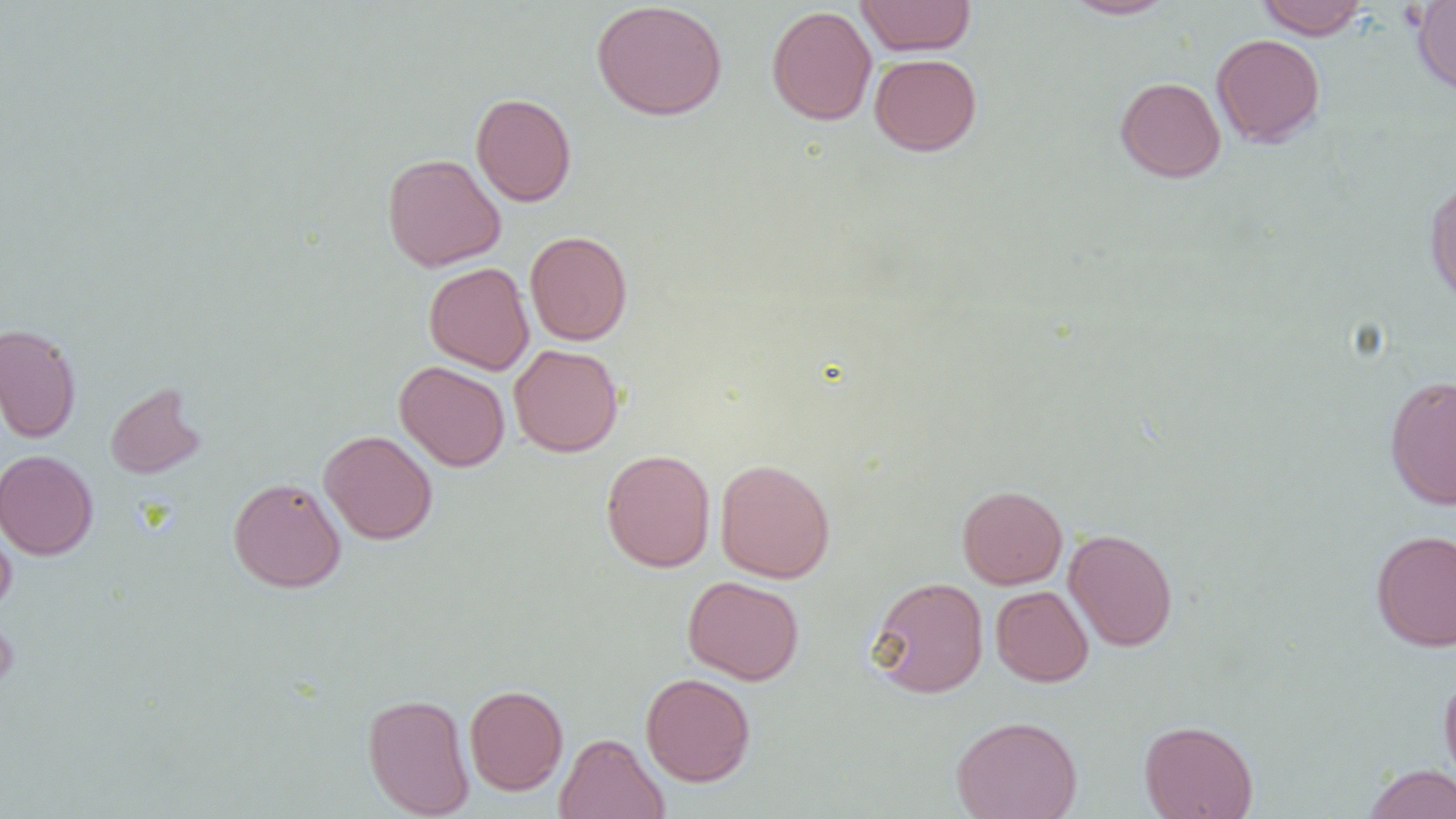

slide-level diagnosis = no evidence of blood parasites
magnification = 1000x
uninfected red blood cell locations = approximate bounding boxes as (x1, y1, x2, y2) in pixels: (856, 0, 976, 56), (1061, 0, 1176, 19), (1256, 0, 1371, 39), (591, 1, 728, 121), (1411, 1, 1456, 95), (766, 5, 877, 126), (1211, 33, 1325, 147), (869, 53, 982, 156), (1115, 76, 1226, 183), (471, 92, 576, 207), (381, 153, 506, 271), (1423, 178, 1456, 304), (525, 230, 632, 346), (424, 262, 534, 374), (0, 322, 81, 443), (508, 343, 624, 457), (395, 360, 510, 472), (1385, 375, 1456, 510), (105, 381, 207, 479), (319, 430, 437, 544), (601, 448, 716, 573), (0, 449, 98, 560), (714, 458, 835, 582), (228, 477, 346, 592), (957, 485, 1068, 589), (0, 515, 17, 617), (1064, 528, 1178, 652), (1370, 529, 1456, 652), (682, 575, 804, 685), (867, 576, 989, 698), (990, 585, 1093, 687), (0, 613, 19, 695), (1439, 670, 1456, 791), (641, 672, 756, 787), (464, 684, 568, 795), (363, 693, 475, 818), (951, 715, 1082, 819), (1139, 719, 1258, 819), (554, 733, 668, 819), (1363, 763, 1456, 819)
field of view = one of a larger specimen
modality = optical microscopy
image size = 1456×819 pixels
preparation = thin blood smear